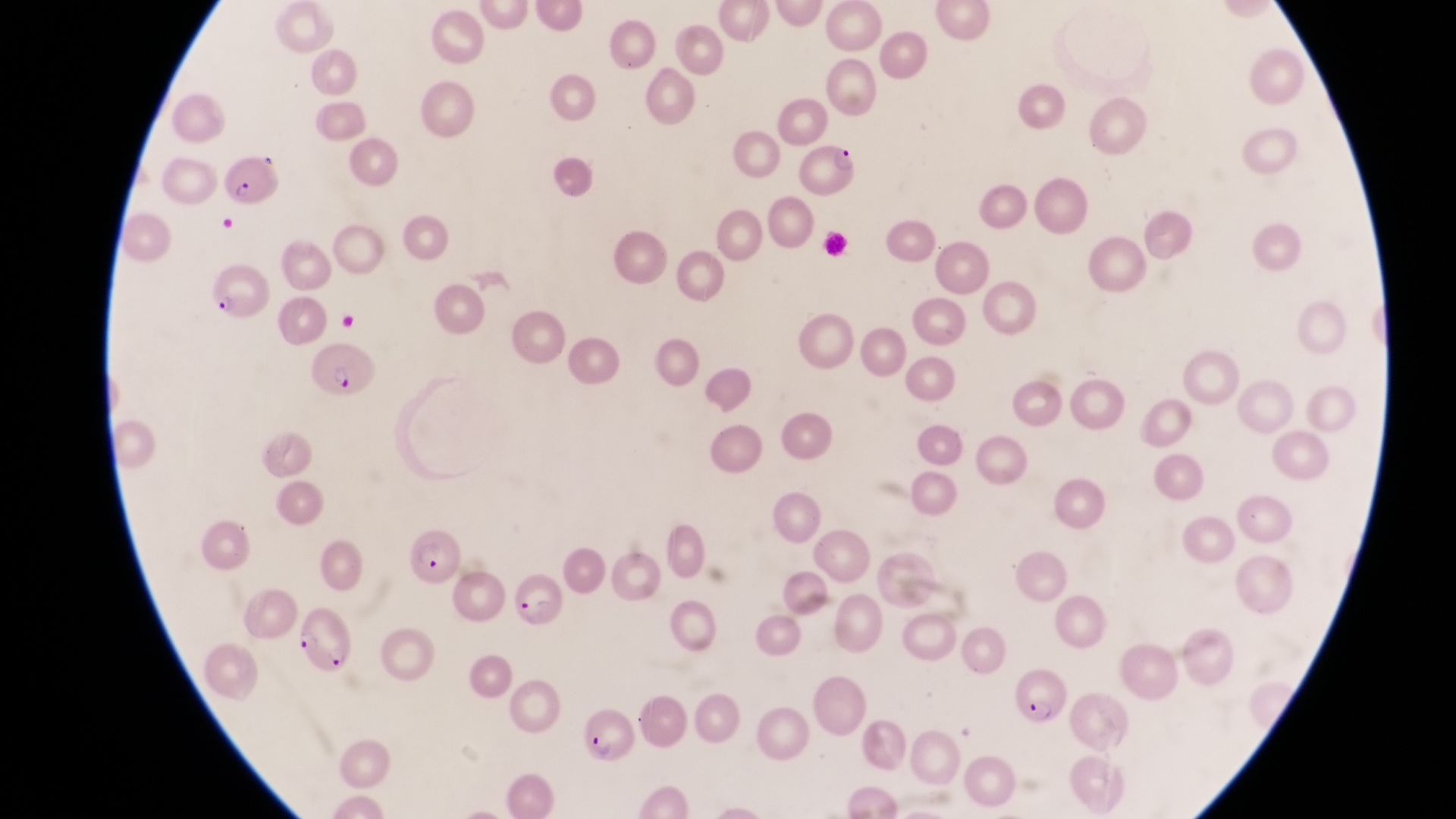
capture = smartphone photograph through the eyepiece of an Olympus CX-23 microscope
image size = 1456×819 pixels
magnification = 1000x
preparation = thin blood smear
field of view = single
country = Uganda
parasitised red blood cell locations = approximate bounding boxes as left top right bottom in pixels: 798 138 859 196; 218 153 279 206; 208 267 272 327; 307 341 374 404; 406 531 464 589; 512 571 568 630; 291 601 354 674; 1012 661 1068 730; 579 710 631 763